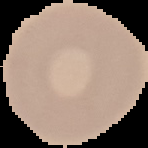

Result: no Plasmodium parasites detected. Image is 148×148 pixels. From a thin blood smear. Segmented cell region on a black background.